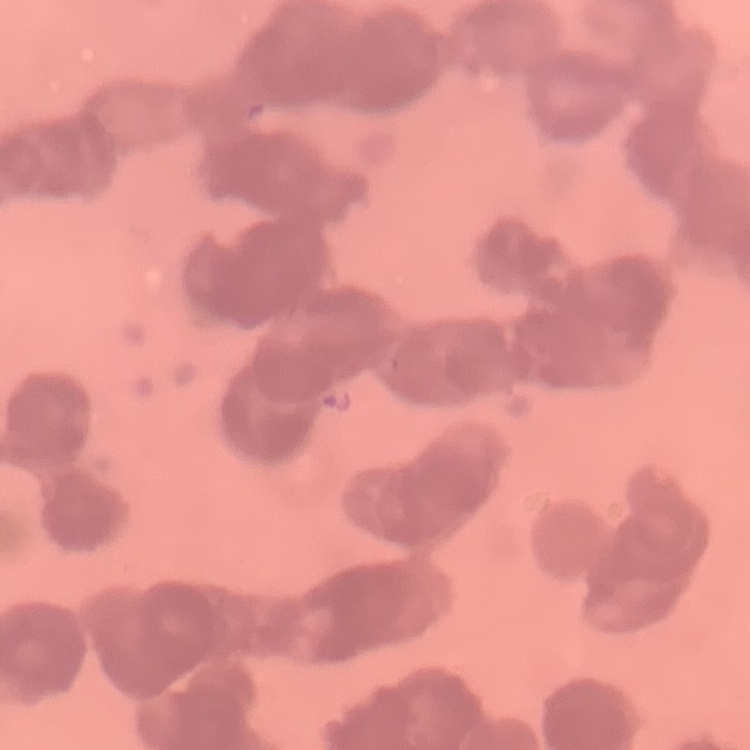

{
  "red_blood_cell_morphology": "rouleaux formation",
  "image_type": "one tile cut from a larger photomicrograph",
  "stain": "Field's or Giemsa",
  "preparation": "thin peripheral smear"
}